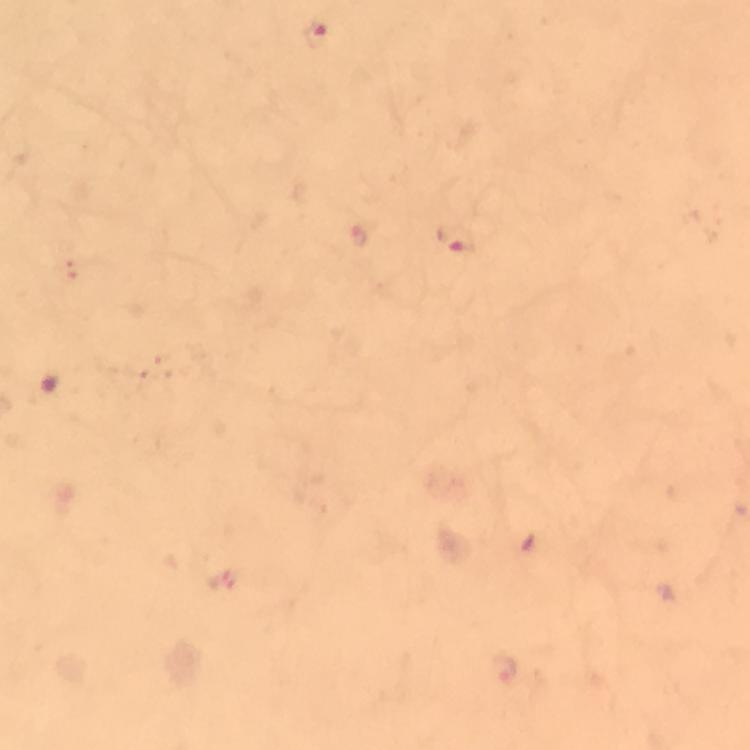
Approximate centers as [x, y] in pixels. Malaria parasite locations: [314, 33], [454, 239]. Image is 750×750 pixels. At 100x magnification. From a malaria diagnostic workup. Giemsa-stained preparation. Cropped region of a single field of view. Immersion oil applied. Thick blood smear. Photographed with a smartphone mounted on the microscope.